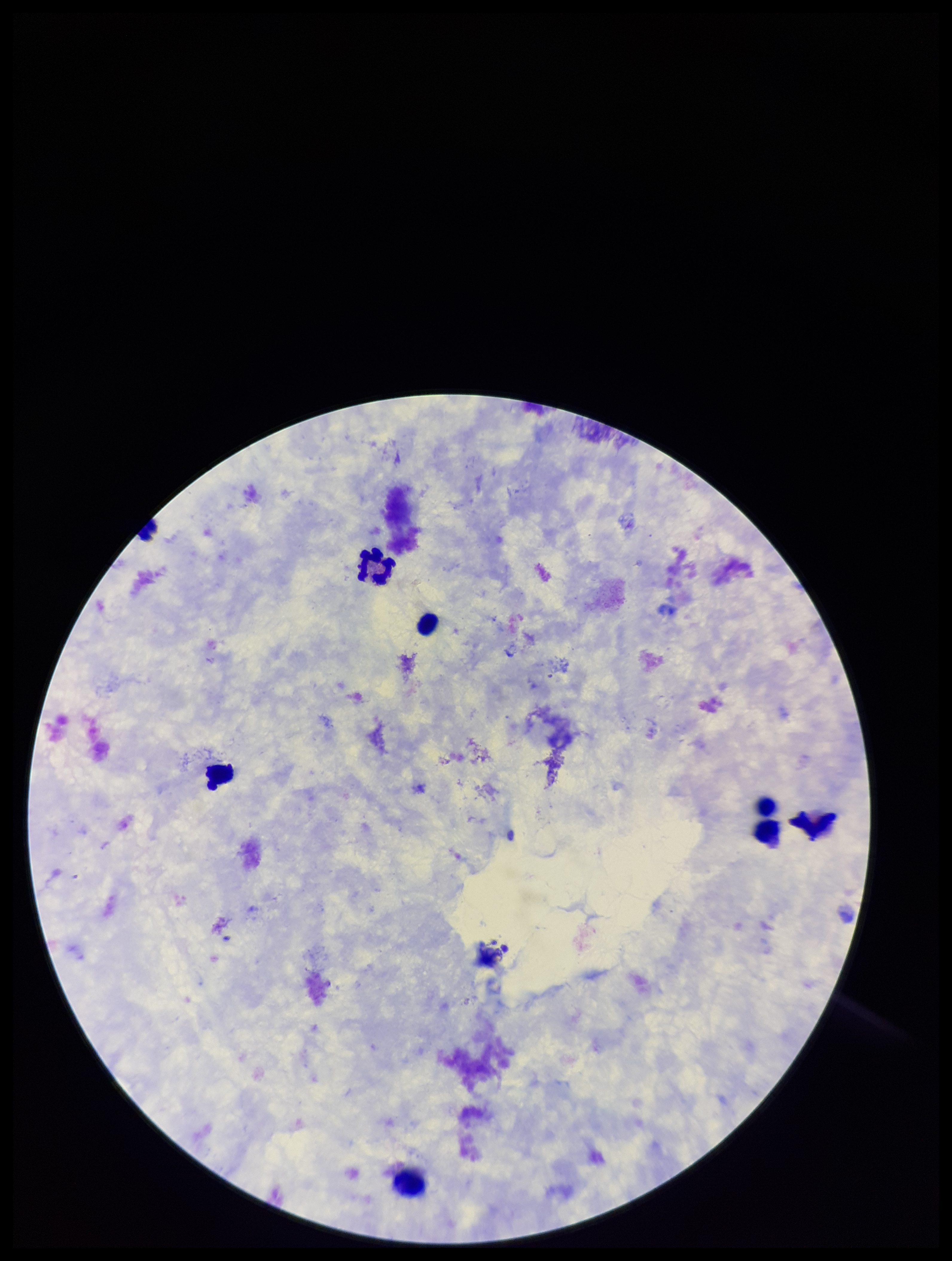 Parasite count: 0. Image is 952×1261 pixels. Leukocyte count: 8. Smartphone photograph taken through the eyepiece of a microscope. One field from this slide. Giemsa stain. Plasmodium parasites: none detected. Preparation: thick. Patient malaria status: negative.